Assess this cell for malaria.
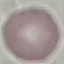

Uninfected.

Automatically extracted cell patch, resized to 64 × 64 pixels. Thin blood smear. Giemsa stain. Acquired by smartphone through the microscope eyepiece.